Assess this cell for malaria.
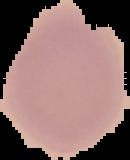
Uninfected.

Summary:
  - Preparation: thin blood film
  - Image size: 130×160 pixels
  - Image type: segmented cell region on a black background